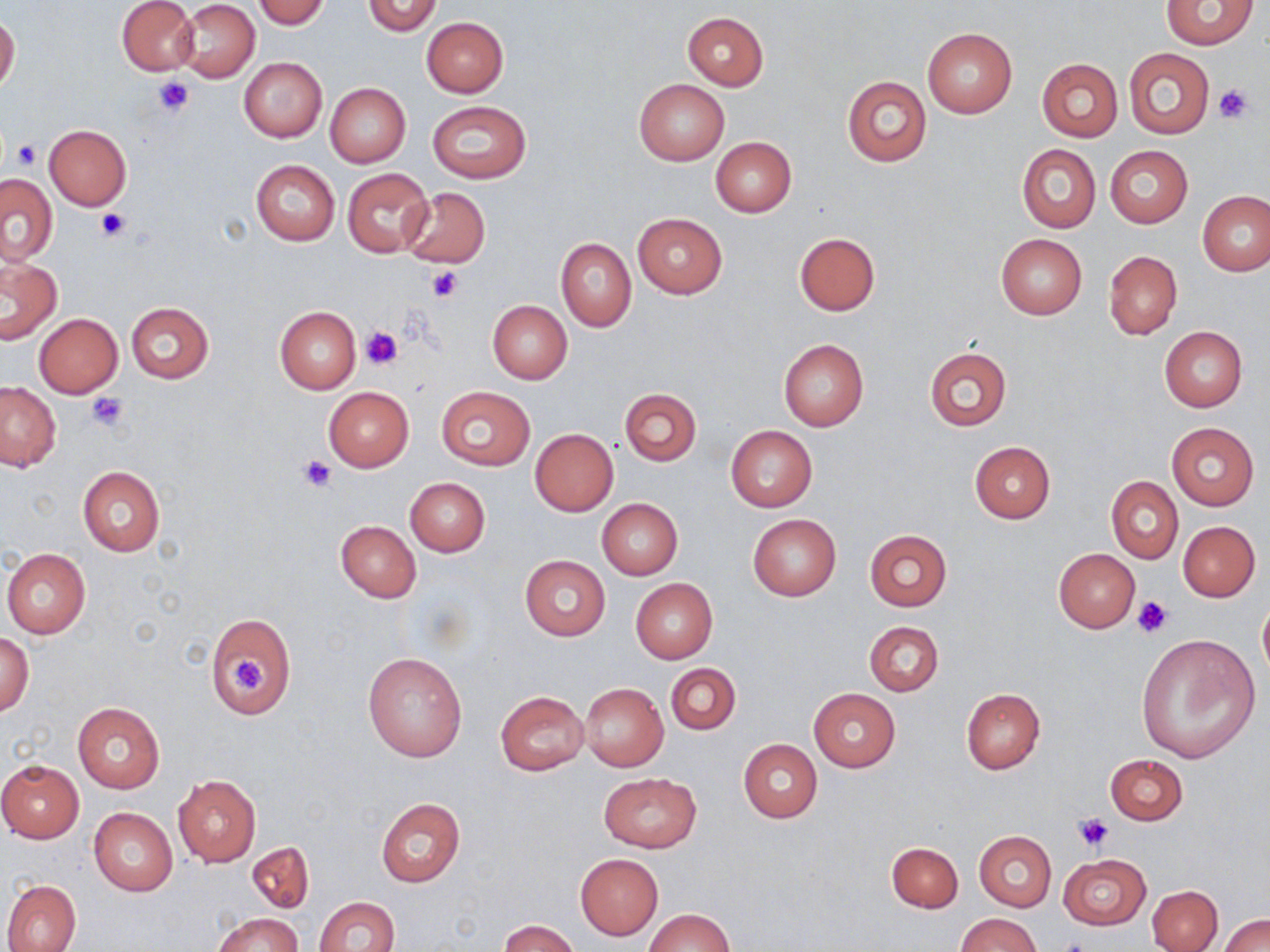

slide-level diagnosis = no evidence of blood parasites
image size = 1270×952 pixels
stain = May-Grünwald-Giemsa
magnification = 1000x
field of view = single
uninfected red blood cell locations = approximate bounding boxes as (x1,y1)-(x2,y2) corner pairs in pixels: (116,0)-(199,76), (362,0)-(442,36), (1162,0)-(1260,49), (175,1)-(259,82), (253,1)-(331,27), (682,12)-(769,90), (0,15)-(20,95), (421,17)-(509,97), (923,27)-(1017,119), (1124,48)-(1214,139), (239,58)-(326,142), (1037,58)-(1122,142), (841,76)-(931,168), (634,79)-(729,166), (326,83)-(411,167), (427,100)-(531,183), (43,123)-(132,211), (710,138)-(796,217), (1104,144)-(1193,228), (1017,145)-(1101,232), (251,159)-(340,246), (342,168)-(434,256), (0,173)-(58,265), (400,188)-(490,269), (1198,191)-(1270,276), (634,212)-(727,298), (795,232)-(880,315), (995,233)-(1089,319), (556,239)-(636,331), (1103,250)-(1182,341), (1,255)-(63,344), (486,300)-(572,384), (126,303)-(213,383), (275,306)-(360,393), (34,313)-(123,398), (1160,326)-(1247,411), (778,338)-(869,431), (922,346)-(1013,433), (0,382)-(61,472), (435,386)-(535,470), (323,387)-(413,471), (620,387)-(701,466), (1166,421)-(1259,510), (726,426)-(817,512), (530,429)-(618,515), (970,441)-(1056,523), (77,466)-(165,557), (1107,476)-(1182,563), (405,477)-(490,557), (598,499)-(682,579), (748,514)-(841,600), (335,521)-(421,602), (1178,521)-(1260,601), (864,529)-(952,611), (2,549)-(90,638), (1053,549)-(1140,632), (519,554)-(611,641), (630,578)-(717,663), (1258,597)-(1270,685), (205,612)-(297,718), (864,621)-(944,696), (2,630)-(34,717), (1136,634)-(1261,763), (363,652)-(467,761), (666,663)-(740,735), (580,683)-(669,771), (961,688)-(1046,773), (807,689)-(900,771), (495,690)-(589,774), (72,702)-(165,794), (739,740)-(821,823), (1105,754)-(1187,826), (0,759)-(85,842), (599,773)-(702,853), (172,775)-(261,866), (374,798)-(465,888), (88,807)-(178,896), (975,831)-(1056,911), (247,842)-(314,913), (886,842)-(962,913), (575,853)-(663,939), (1058,855)-(1151,928), (3,879)-(81,952), (1148,884)-(1222,952), (313,897)-(401,952), (646,909)-(734,952), (212,913)-(301,952), (958,913)-(1040,952), (1220,914)-(1270,952), (502,919)-(578,952)
modality = light microscopy
preparation = thin blood film
platelet locations = approximate bounding boxes as (x1,y1)-(x2,y2) corner pairs in pixels: (153,76)-(198,119), (1213,84)-(1256,124), (12,141)-(41,167), (95,207)-(132,242), (425,266)-(461,302), (363,327)-(401,368), (88,392)-(130,432), (299,455)-(337,492), (1131,595)-(1173,637), (229,655)-(268,694), (1074,813)-(1115,852)